Outline each blood parasite and name the species.
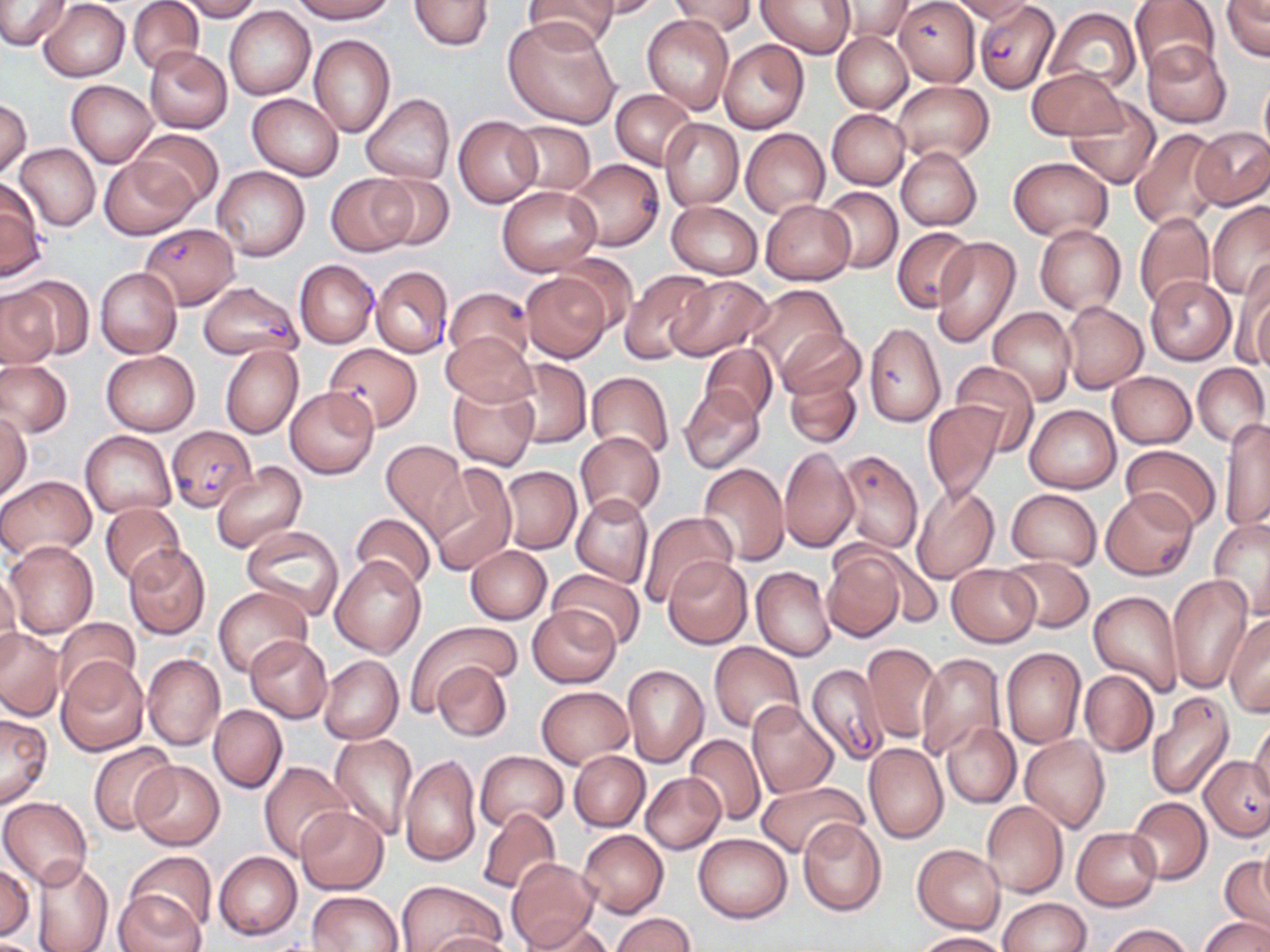

Approximate bounding boxes as named x1/y1/x2/y2 corners in pixels.
Plasmodium falciparum-infected red blood cells: (x1=975, y1=2, x2=1059, y2=94), (x1=141, y1=223, x2=240, y2=309), (x1=291, y1=263, x2=380, y2=353), (x1=373, y1=270, x2=452, y2=361), (x1=198, y1=280, x2=301, y2=360), (x1=166, y1=425, x2=257, y2=511), (x1=806, y1=664, x2=889, y2=767).
No Plasmodium ovale, Plasmodium malariae, Plasmodium vivax, Babesia divergens, or Trypanosoma brucei observed.

Summary:
  - Uninfected red blood cell locations: (x1=0, y1=0, x2=71, y2=50), (x1=127, y1=0, x2=203, y2=73), (x1=174, y1=0, x2=262, y2=21), (x1=289, y1=0, x2=396, y2=23), (x1=408, y1=0, x2=493, y2=51), (x1=522, y1=0, x2=619, y2=51), (x1=586, y1=0, x2=662, y2=19), (x1=669, y1=0, x2=757, y2=37), (x1=759, y1=0, x2=854, y2=57), (x1=895, y1=0, x2=981, y2=86), (x1=951, y1=0, x2=1034, y2=23), (x1=1128, y1=0, x2=1221, y2=79), (x1=1220, y1=0, x2=1270, y2=61), (x1=37, y1=1, x2=130, y2=81), (x1=834, y1=1, x2=913, y2=42), (x1=224, y1=6, x2=316, y2=99), (x1=1044, y1=8, x2=1140, y2=93), (x1=642, y1=14, x2=735, y2=116), (x1=504, y1=18, x2=621, y2=129), (x1=832, y1=31, x2=912, y2=114), (x1=308, y1=34, x2=395, y2=138), (x1=719, y1=40, x2=810, y2=135), (x1=1142, y1=40, x2=1231, y2=128), (x1=143, y1=47, x2=232, y2=134), (x1=1026, y1=67, x2=1127, y2=140), (x1=1259, y1=74, x2=1270, y2=159), (x1=66, y1=80, x2=159, y2=167), (x1=892, y1=81, x2=994, y2=164), (x1=610, y1=88, x2=696, y2=168), (x1=247, y1=93, x2=344, y2=180), (x1=361, y1=93, x2=454, y2=185), (x1=1065, y1=97, x2=1161, y2=188), (x1=0, y1=98, x2=31, y2=177), (x1=827, y1=109, x2=909, y2=190), (x1=453, y1=115, x2=542, y2=209), (x1=659, y1=118, x2=743, y2=210), (x1=507, y1=120, x2=596, y2=195), (x1=1131, y1=127, x2=1222, y2=230), (x1=1191, y1=127, x2=1270, y2=210), (x1=132, y1=128, x2=223, y2=209), (x1=741, y1=128, x2=830, y2=217), (x1=14, y1=143, x2=100, y2=230), (x1=896, y1=146, x2=982, y2=231), (x1=100, y1=156, x2=196, y2=240), (x1=1008, y1=156, x2=1112, y2=240), (x1=572, y1=163, x2=667, y2=256), (x1=211, y1=166, x2=310, y2=261), (x1=325, y1=174, x2=418, y2=257), (x1=370, y1=174, x2=454, y2=250), (x1=0, y1=181, x2=46, y2=280), (x1=497, y1=185, x2=601, y2=276), (x1=820, y1=185, x2=902, y2=273), (x1=759, y1=200, x2=855, y2=284), (x1=666, y1=201, x2=763, y2=279), (x1=1206, y1=202, x2=1270, y2=298), (x1=1134, y1=211, x2=1215, y2=312), (x1=1034, y1=224, x2=1125, y2=315), (x1=892, y1=226, x2=973, y2=311), (x1=930, y1=237, x2=1022, y2=348), (x1=555, y1=254, x2=638, y2=333), (x1=1234, y1=263, x2=1270, y2=371), (x1=95, y1=267, x2=182, y2=358), (x1=622, y1=270, x2=714, y2=361), (x1=521, y1=272, x2=612, y2=363), (x1=11, y1=275, x2=94, y2=358), (x1=667, y1=276, x2=772, y2=361), (x1=1145, y1=276, x2=1237, y2=366), (x1=747, y1=283, x2=848, y2=375), (x1=445, y1=287, x2=533, y2=366), (x1=0, y1=288, x2=61, y2=370), (x1=1062, y1=301, x2=1148, y2=393), (x1=989, y1=307, x2=1075, y2=406), (x1=864, y1=321, x2=946, y2=428), (x1=779, y1=330, x2=865, y2=403), (x1=442, y1=332, x2=536, y2=407), (x1=323, y1=342, x2=423, y2=432), (x1=220, y1=344, x2=302, y2=439), (x1=700, y1=345, x2=778, y2=422), (x1=101, y1=350, x2=200, y2=435), (x1=503, y1=358, x2=591, y2=449), (x1=0, y1=360, x2=72, y2=438), (x1=950, y1=361, x2=1039, y2=456), (x1=1193, y1=363, x2=1269, y2=446), (x1=784, y1=370, x2=862, y2=448), (x1=586, y1=371, x2=674, y2=458), (x1=1107, y1=371, x2=1196, y2=447), (x1=448, y1=383, x2=539, y2=471), (x1=678, y1=385, x2=766, y2=475), (x1=285, y1=386, x2=379, y2=478), (x1=922, y1=400, x2=1004, y2=507), (x1=1026, y1=405, x2=1120, y2=493), (x1=0, y1=413, x2=31, y2=498), (x1=1218, y1=418, x2=1270, y2=533), (x1=575, y1=431, x2=665, y2=519), (x1=81, y1=432, x2=175, y2=517), (x1=379, y1=439, x2=469, y2=534), (x1=1120, y1=446, x2=1222, y2=533), (x1=779, y1=447, x2=857, y2=553), (x1=834, y1=448, x2=924, y2=554), (x1=726, y1=450, x2=831, y2=561), (x1=211, y1=461, x2=307, y2=553), (x1=425, y1=463, x2=518, y2=576), (x1=696, y1=463, x2=788, y2=565), (x1=501, y1=466, x2=581, y2=555), (x1=0, y1=474, x2=96, y2=560), (x1=671, y1=486, x2=777, y2=595), (x1=912, y1=486, x2=999, y2=584), (x1=1006, y1=489, x2=1101, y2=568), (x1=1103, y1=491, x2=1196, y2=578), (x1=571, y1=494, x2=653, y2=588), (x1=101, y1=502, x2=186, y2=587), (x1=640, y1=513, x2=738, y2=605), (x1=350, y1=514, x2=436, y2=593), (x1=1208, y1=518, x2=1270, y2=618), (x1=241, y1=525, x2=347, y2=622), (x1=5, y1=540, x2=98, y2=638), (x1=123, y1=543, x2=212, y2=639), (x1=466, y1=545, x2=551, y2=624), (x1=823, y1=548, x2=906, y2=642), (x1=331, y1=555, x2=426, y2=657), (x1=999, y1=556, x2=1093, y2=633), (x1=662, y1=557, x2=753, y2=649), (x1=947, y1=564, x2=1040, y2=647), (x1=751, y1=566, x2=835, y2=661), (x1=549, y1=568, x2=647, y2=650), (x1=0, y1=569, x2=20, y2=652), (x1=1166, y1=572, x2=1253, y2=692), (x1=214, y1=586, x2=311, y2=678), (x1=1089, y1=590, x2=1182, y2=697), (x1=529, y1=606, x2=622, y2=688), (x1=1224, y1=615, x2=1270, y2=716), (x1=55, y1=617, x2=140, y2=696), (x1=408, y1=622, x2=518, y2=709), (x1=0, y1=628, x2=66, y2=721), (x1=244, y1=635, x2=332, y2=722), (x1=709, y1=642, x2=803, y2=734), (x1=860, y1=642, x2=942, y2=745), (x1=1001, y1=648, x2=1086, y2=748), (x1=915, y1=652, x2=1004, y2=761), (x1=142, y1=653, x2=225, y2=750), (x1=319, y1=654, x2=403, y2=744), (x1=56, y1=656, x2=149, y2=755), (x1=432, y1=662, x2=512, y2=742), (x1=621, y1=665, x2=709, y2=766), (x1=1080, y1=669, x2=1157, y2=757), (x1=536, y1=687, x2=632, y2=767), (x1=1146, y1=692, x2=1234, y2=800), (x1=746, y1=700, x2=838, y2=799), (x1=209, y1=705, x2=287, y2=794), (x1=0, y1=711, x2=52, y2=809), (x1=1248, y1=721, x2=1270, y2=804), (x1=941, y1=723, x2=1021, y2=809), (x1=329, y1=733, x2=417, y2=839), (x1=685, y1=734, x2=766, y2=825), (x1=1021, y1=734, x2=1110, y2=833), (x1=88, y1=742, x2=179, y2=833), (x1=864, y1=742, x2=948, y2=843), (x1=475, y1=751, x2=568, y2=830), (x1=569, y1=751, x2=649, y2=831), (x1=400, y1=754, x2=482, y2=868), (x1=1200, y1=757, x2=1269, y2=840), (x1=131, y1=760, x2=224, y2=850), (x1=258, y1=761, x2=351, y2=861), (x1=641, y1=773, x2=725, y2=853), (x1=756, y1=780, x2=867, y2=860), (x1=1, y1=797, x2=92, y2=887), (x1=1126, y1=797, x2=1212, y2=885), (x1=980, y1=801, x2=1068, y2=898), (x1=295, y1=806, x2=389, y2=894), (x1=477, y1=806, x2=563, y2=895), (x1=797, y1=818, x2=888, y2=917), (x1=1072, y1=827, x2=1161, y2=911), (x1=578, y1=829, x2=668, y2=918), (x1=694, y1=833, x2=791, y2=923), (x1=1257, y1=839, x2=1270, y2=921), (x1=912, y1=844, x2=1005, y2=934), (x1=125, y1=850, x2=215, y2=936), (x1=213, y1=850, x2=302, y2=941), (x1=506, y1=857, x2=597, y2=951), (x1=1218, y1=857, x2=1269, y2=937), (x1=29, y1=859, x2=113, y2=952), (x1=0, y1=860, x2=34, y2=941), (x1=396, y1=882, x2=504, y2=952), (x1=113, y1=890, x2=206, y2=952), (x1=307, y1=891, x2=403, y2=951), (x1=997, y1=898, x2=1089, y2=952), (x1=611, y1=911, x2=696, y2=951), (x1=1200, y1=916, x2=1269, y2=952), (x1=520, y1=920, x2=615, y2=951), (x1=1104, y1=924, x2=1194, y2=952), (x1=420, y1=930, x2=517, y2=952), (x1=911, y1=932, x2=1009, y2=951)
  - Slide-level diagnosis: Plasmodium falciparum
  - Field of view: one of a larger specimen
  - Modality: light microscopy
  - Image size: 1270×952 pixels
  - Stain: May-Grünwald-Giemsa
  - Preparation: thin blood smear
  - Magnification: 1000x